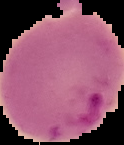

{
  "malaria_status": "parasitized",
  "preparation": "thin blood film",
  "image_type": "segmented cell region on a black background",
  "image_size": "124×145 pixels"
}